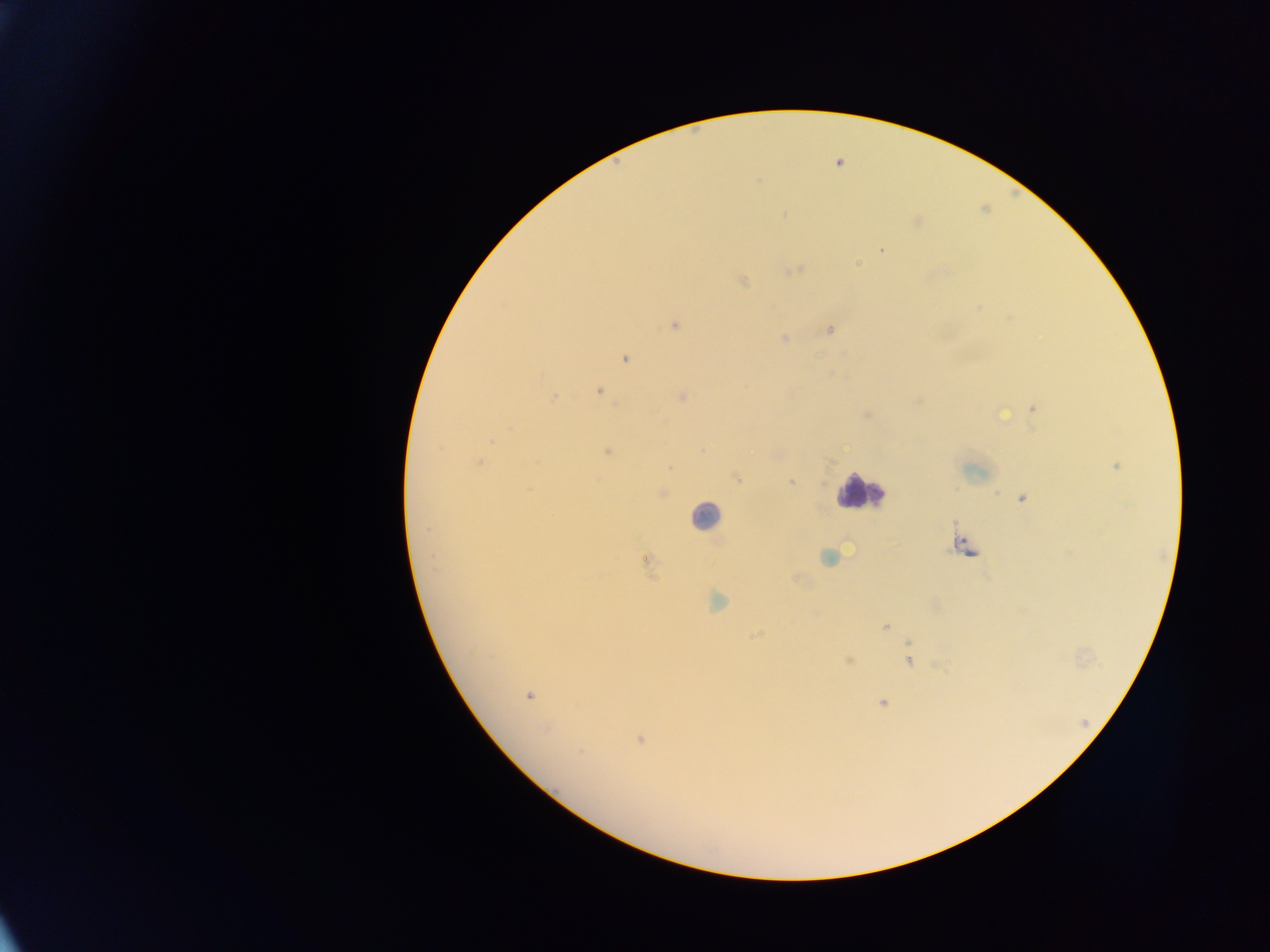 Approximate centers as x y in pixels. Malaria parasite locations: 839 162; 881 250; 858 263; 796 270; 742 280; 674 325; 830 329; 783 338; 625 358; 598 391; 553 397; 682 397; 1034 410; 1003 413; 702 451; 607 452; 478 462; 1115 466; 737 477; 791 482; 663 492; 1021 498; 961 543; 829 557; 645 560; 717 600; 884 627; 756 634; 849 660; 909 660; 528 696; 883 703; 639 740; 580 752. Leukocyte locations: 860 491; 705 516. Photographed through a microscope with a mobile-phone camera. One field of view. Thick blood smear. Image is 1270×952 pixels. Sample from Ghana.